State which parasite is depicted.
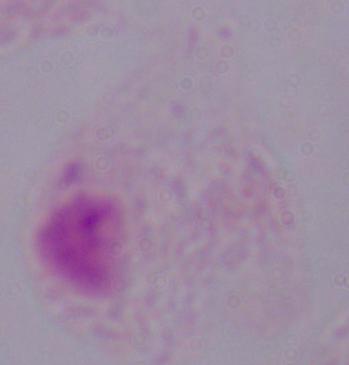
A trichomonad.

magnification = 1000x
modality = micrograph